Outline each blood parasite and name the species.
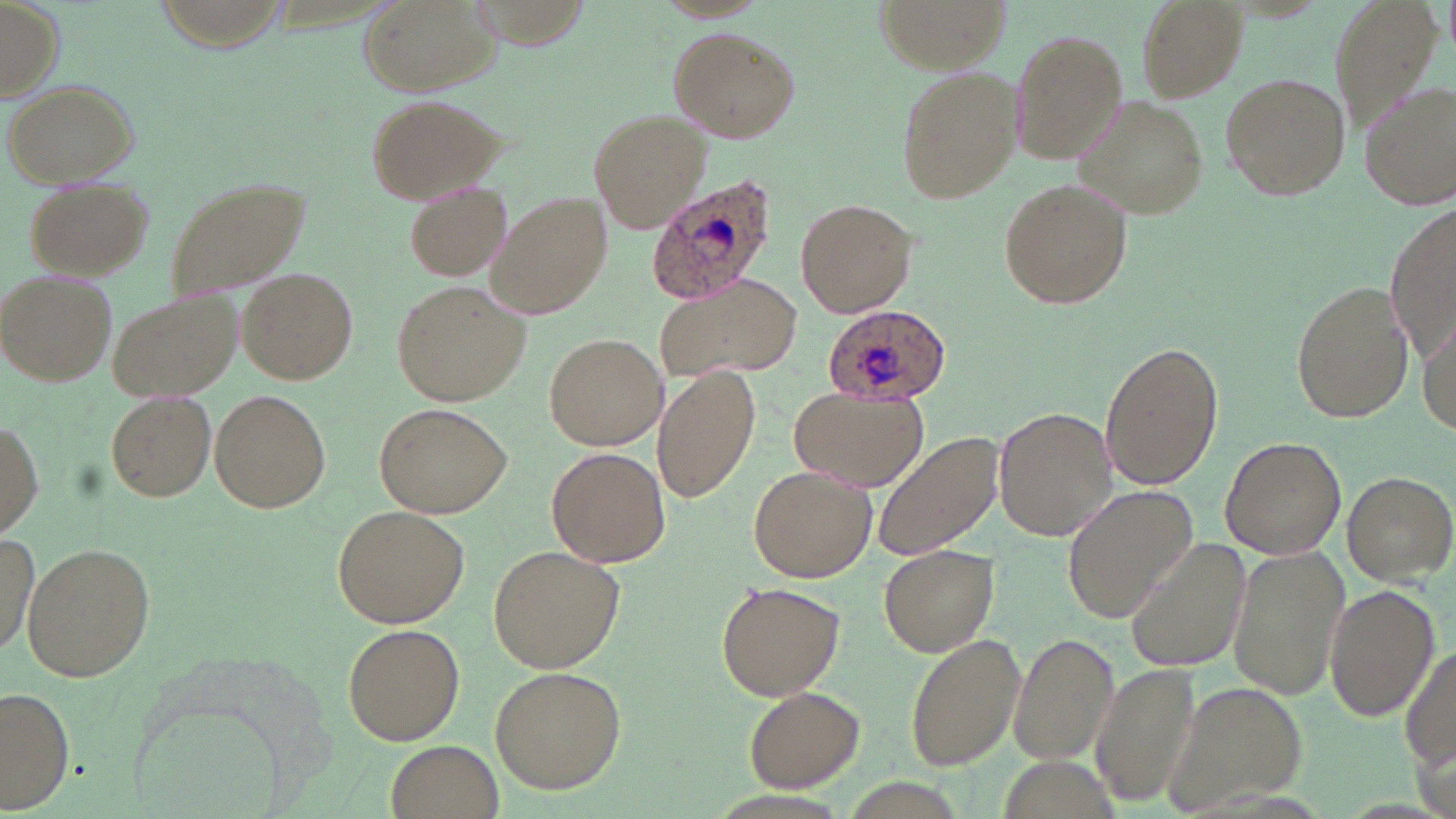
Approximate bounding boxes as [x1, y1, x2, y2] in pixels.
Plasmodium ovale-infected red blood cells: [646, 174, 779, 305], [822, 304, 952, 404].
No Plasmodium falciparum, Plasmodium malariae, Plasmodium vivax, Babesia divergens, or Trypanosoma brucei observed.

Summary:
  - Uninfected red blood cell locations: [356, 0, 503, 98], [876, 0, 1009, 70], [1135, 0, 1247, 100], [0, 2, 64, 102], [668, 26, 800, 143], [1010, 28, 1128, 165], [894, 61, 1024, 204], [1218, 71, 1352, 203], [4, 79, 139, 187], [1357, 80, 1455, 209], [365, 94, 510, 204], [1078, 95, 1206, 218], [588, 109, 709, 233], [162, 176, 310, 303], [997, 176, 1133, 310], [25, 178, 152, 277], [404, 181, 514, 281], [488, 192, 613, 319], [794, 196, 916, 318], [1387, 196, 1456, 371], [238, 268, 357, 383], [2, 271, 117, 388], [655, 272, 803, 380], [1290, 277, 1413, 424], [390, 280, 530, 407], [107, 290, 241, 404], [1418, 314, 1456, 444], [544, 331, 667, 450], [1099, 339, 1225, 490], [654, 366, 759, 502], [789, 387, 928, 491], [209, 390, 331, 515], [105, 391, 217, 503], [375, 400, 514, 517], [995, 404, 1116, 542], [0, 420, 42, 541], [872, 431, 1005, 562], [1221, 433, 1348, 560], [548, 448, 670, 567], [746, 465, 876, 583], [1341, 470, 1454, 583], [1066, 488, 1196, 620], [333, 504, 470, 627], [1, 533, 40, 667], [1124, 537, 1253, 673], [22, 542, 155, 684], [487, 543, 626, 674], [879, 544, 1001, 655], [1227, 549, 1349, 701], [714, 579, 845, 699], [1324, 584, 1438, 724], [342, 624, 466, 746], [905, 632, 1025, 771], [1009, 633, 1119, 767], [1401, 641, 1454, 781], [1092, 662, 1200, 810], [488, 666, 626, 793], [1160, 679, 1309, 816], [2, 686, 75, 813], [741, 687, 866, 790], [388, 741, 503, 817]
  - Slide-level diagnosis: Plasmodium ovale
  - Stain: May-Grünwald-Giemsa
  - Image size: 1456×819 pixels
  - Preparation: thin blood smear
  - Modality: light microscopy
  - Magnification: 1000x
  - Field of view: one of a larger specimen